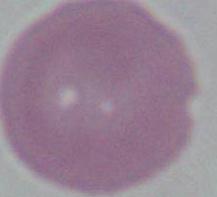

Summary:
  - Identification: erythrocyte
  - Modality: micrograph
  - Magnification: 1000x